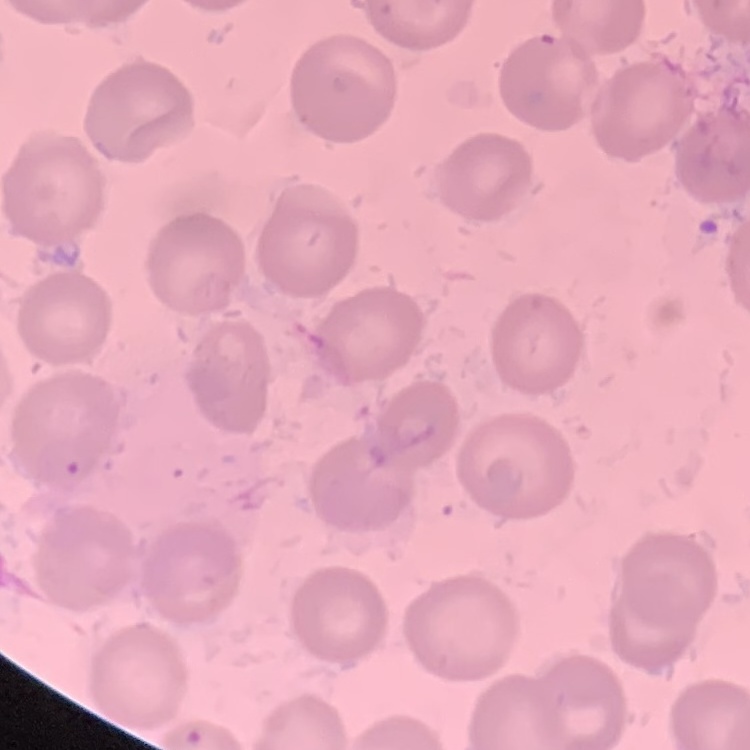
red_blood_cell_morphology: no rouleaux formation
preparation: thin blood film
image_type: square crop of a larger photomicrograph
stain: Field's or Giemsa